Give the position of every Plasmodium parasite.
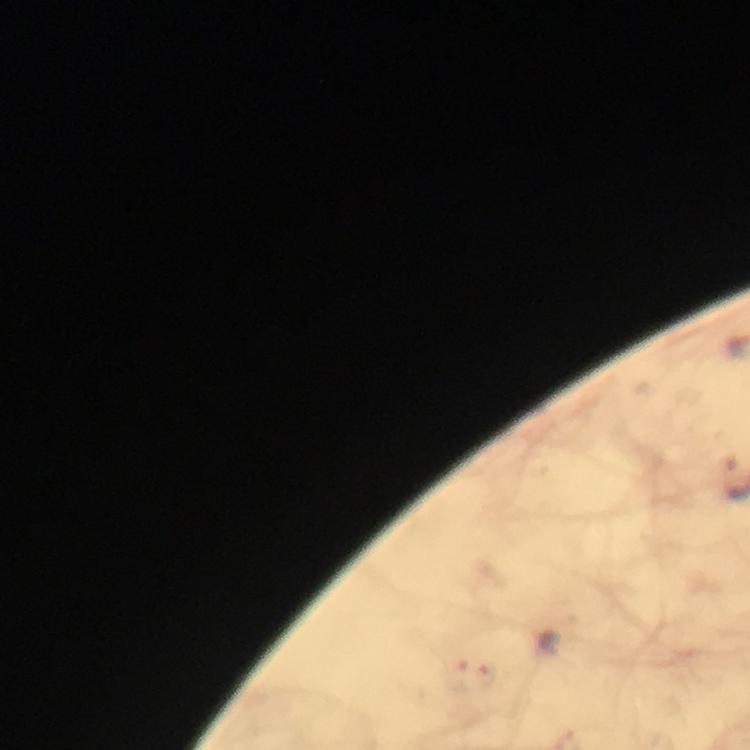
Approximate centers as (x, y) in pixels.
Plasmodium parasites: (487, 676).

Thick smear. 100x magnification. Smartphone photograph taken through a microscope. Cropped region of a single field of view. Giemsa stain. From a malaria diagnostic workup. Immersion oil applied. Image is 750×750 pixels.